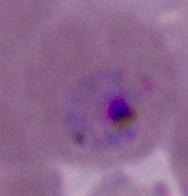
Summary:
  - Modality: photomicrograph
  - Identification: Plasmodium
  - Magnification: 400x or 1000x